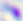

magnification: 400x
modality: photomicrograph
identification: Toxoplasma gondii